Point out each malaria parasite.
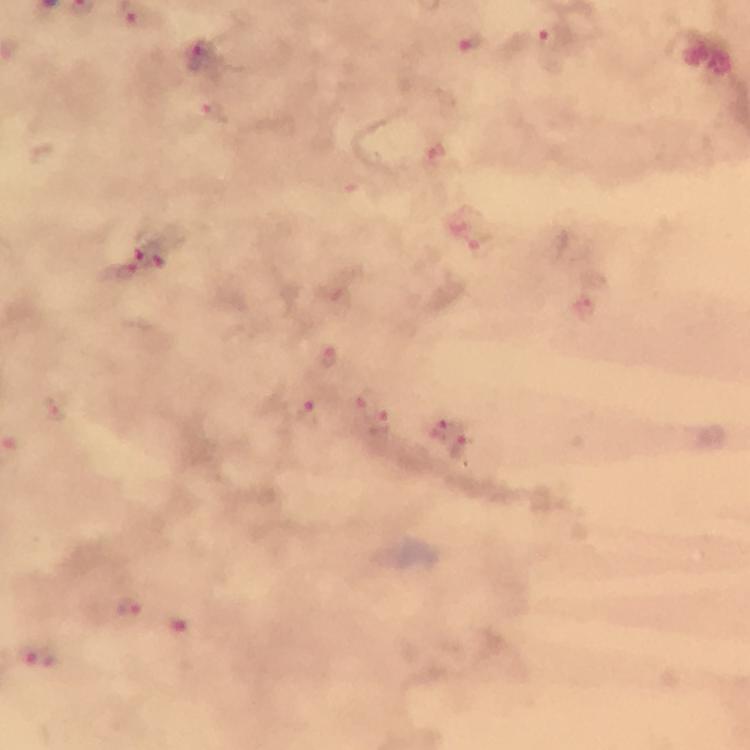
Approximate centers as [x, y] in pixels.
Malaria parasites: [549, 36], [472, 44], [200, 56], [207, 110], [482, 242], [141, 243], [175, 249], [128, 271], [584, 307], [328, 359], [52, 409], [306, 416], [380, 422], [440, 429], [459, 448], [126, 609], [186, 625], [33, 654].

cropped from = one field of view
context = from a diagnostic examination for malaria
preparation = thick blood film
image size = 750×750 pixels
capture = smartphone camera through the microscope
immersion oil = applied
stain = Giemsa
magnification = 100x